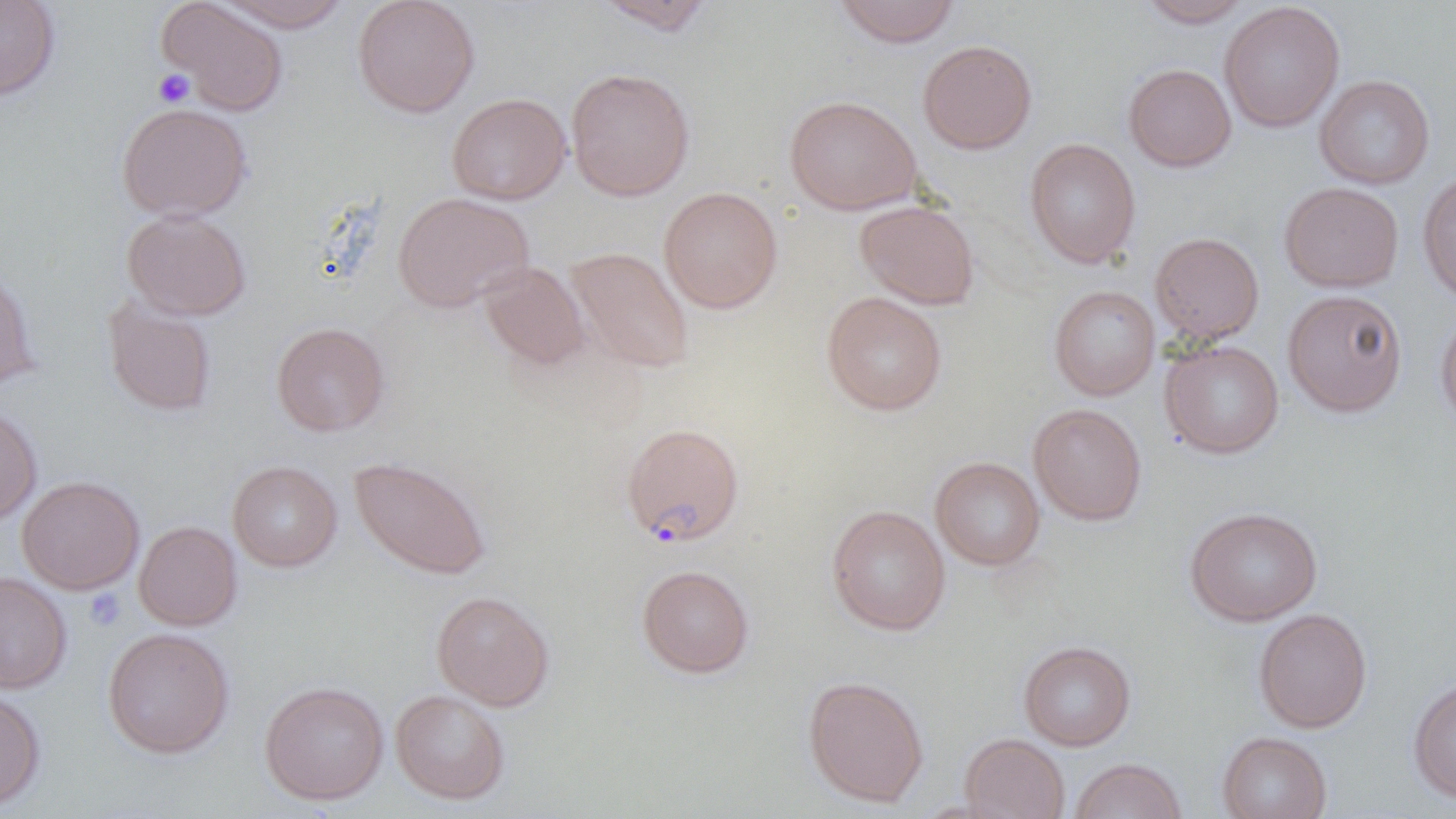

Approximate bounding boxes as (x1,y1)-(x2,y2) corner pairs in pixels. Platelet locations: (152,68)-(195,108), (84,588)-(125,631). Plasmodium falciparum-infected red blood cell locations: (621,422)-(744,547). Uninfected red blood cell locations: (0,0)-(60,102), (212,0)-(353,33), (352,0)-(480,117), (595,0)-(715,35), (833,0)-(961,47), (1137,0)-(1254,27), (156,1)-(288,116), (1219,2)-(1345,132), (918,39)-(1038,154), (1123,63)-(1236,172), (566,67)-(695,201), (1314,75)-(1435,189), (446,93)-(571,205), (784,95)-(922,215), (116,102)-(252,221), (1024,138)-(1141,268), (1417,171)-(1456,305), (1279,182)-(1404,293), (658,186)-(783,313), (392,192)-(534,313), (854,200)-(980,309), (122,209)-(251,321), (1149,232)-(1264,343), (566,247)-(694,373), (479,261)-(590,370), (0,262)-(40,393), (1049,284)-(1160,400), (1283,289)-(1407,417), (821,291)-(947,416), (102,296)-(217,417), (1435,308)-(1456,433), (271,322)-(390,437), (1160,339)-(1284,458), (0,402)-(42,526), (1028,403)-(1147,526), (350,456)-(491,580), (930,456)-(1046,571), (227,460)-(342,572), (16,475)-(145,594), (826,504)-(951,636), (1184,506)-(1323,626), (134,521)-(242,631), (637,564)-(754,678), (0,570)-(72,693), (431,590)-(554,711), (1253,608)-(1372,733), (102,627)-(234,758), (1018,641)-(1136,750), (803,675)-(928,807), (1408,676)-(1456,803), (259,680)-(388,805), (0,687)-(45,810), (390,689)-(510,804), (1217,731)-(1332,819), (960,733)-(1070,819), (1070,758)-(1187,819). Slide-level diagnosis: Plasmodium falciparum. Optical microscopy. One field of a larger specimen. Thin blood smear. Image is 1456×819 pixels. Captured at 1000x magnification.